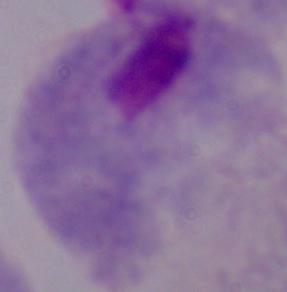 A trichomonad is seen. Photomicrograph. Captured at 1000x magnification.